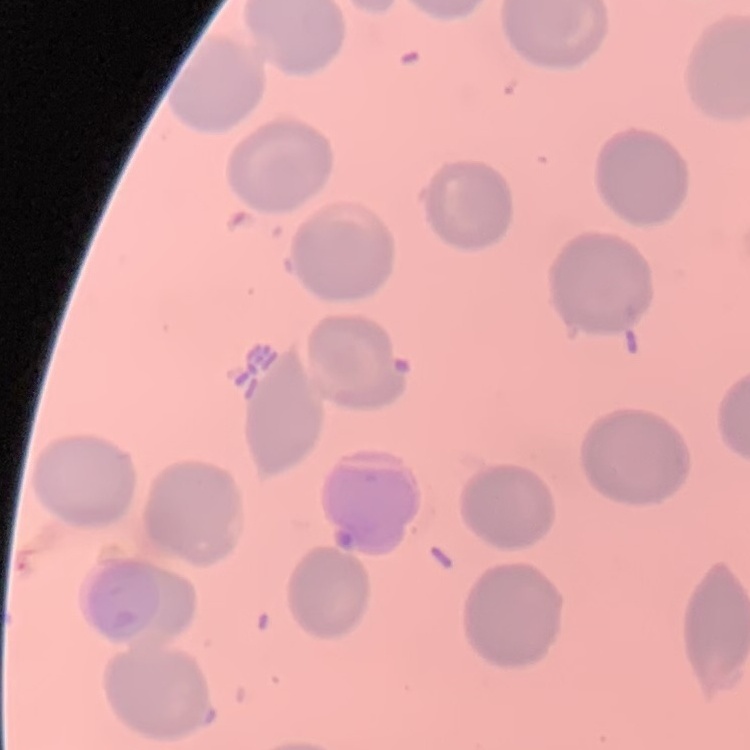

{
  "red_blood_cell_morphology": "no rouleaux formation",
  "image_type": "one tile cut from a larger photomicrograph",
  "preparation": "thin blood film",
  "stain": "Field's or Giemsa"
}